Report the malaria status of this cell.
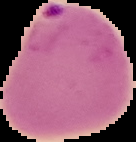
Parasitized.

Segmented cell region on a black background. Image is 136×142 pixels. From a thin blood film.